Identify the parasite.
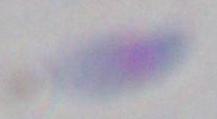

Toxoplasma gondii.

Summary:
  - Magnification: 1000x
  - Modality: photomicrograph